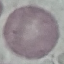

malaria status = uninfected
preparation = thin blood film
capture = smartphone through the microscope eyepiece
image type = cell patch, automatically extracted from a larger field of view and resized to 64 × 64 pixels
stain = Giemsa